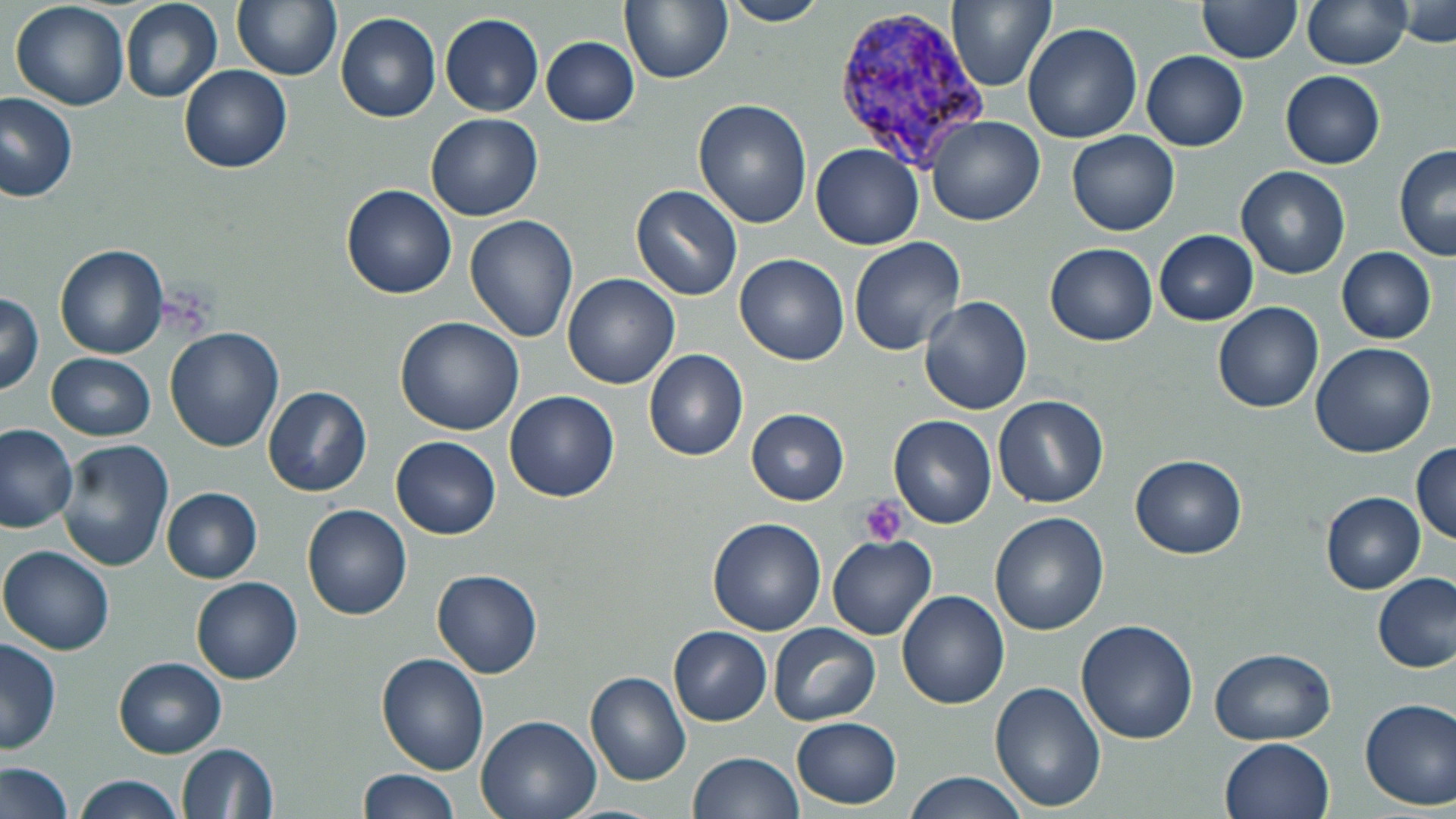

Approximate bounding boxes as (x1,y1)-(x2,y2) corner pairs in pixels. Platelet locations: (860,496)-(909,547). Uninfected red blood cell locations: (231,0)-(341,81), (621,0)-(732,84), (723,0)-(827,26), (949,0)-(1054,90), (1301,0)-(1413,69), (10,1)-(130,112), (121,1)-(223,103), (1398,1)-(1455,47), (1197,2)-(1301,64), (334,13)-(441,122), (441,14)-(543,115), (1023,22)-(1141,142), (541,36)-(640,125), (1142,51)-(1248,150), (180,67)-(292,173), (1281,71)-(1386,168), (0,94)-(78,202), (694,99)-(812,226), (426,114)-(542,220), (926,116)-(1044,225), (1068,130)-(1179,235), (812,143)-(923,249), (1395,145)-(1455,261), (1236,165)-(1352,279), (342,183)-(458,299), (630,184)-(743,301), (824,198)-(948,325), (464,214)-(580,344), (1154,228)-(1259,326), (848,236)-(966,357), (1045,242)-(1157,346), (55,244)-(167,359), (1336,246)-(1438,344), (736,253)-(849,364), (563,275)-(679,390), (0,291)-(44,396), (919,296)-(1032,416), (1213,302)-(1323,413), (395,317)-(525,435), (165,326)-(285,451), (1310,343)-(1436,456), (644,349)-(749,460), (47,351)-(156,441), (263,387)-(372,496), (506,390)-(619,503), (994,395)-(1109,508), (747,408)-(850,504), (888,414)-(998,529), (0,424)-(79,531), (392,437)-(499,539), (58,439)-(175,572), (1411,443)-(1456,543), (1132,454)-(1247,559), (162,488)-(261,582), (1321,492)-(1425,593), (303,504)-(412,619), (991,513)-(1108,636), (708,518)-(827,636), (827,534)-(937,639), (1,544)-(116,655), (432,569)-(543,678), (1373,573)-(1454,672), (192,576)-(302,684), (897,591)-(1008,710), (1076,619)-(1198,744), (770,622)-(881,725), (669,626)-(771,725), (1,635)-(63,754), (1207,648)-(1337,744), (376,653)-(490,774), (115,657)-(226,758), (585,672)-(692,786), (990,682)-(1104,809), (1360,697)-(1456,810), (476,714)-(601,819), (791,716)-(903,809), (1220,738)-(1334,819), (177,743)-(278,818), (690,751)-(804,818), (0,761)-(75,819), (357,768)-(465,819), (902,771)-(1028,819), (75,775)-(186,819), (554,805)-(668,819). Plasmodium vivax-infected red blood cell locations: (832,4)-(994,172). Slide-level diagnosis: Plasmodium vivax. Light microscopy. Image is 1456×819 pixels. May-Grünwald-Giemsa stain. Captured at 1000x magnification. One field of a larger specimen. Thin blood smear.